Comment on the morphology of the red blood cells.
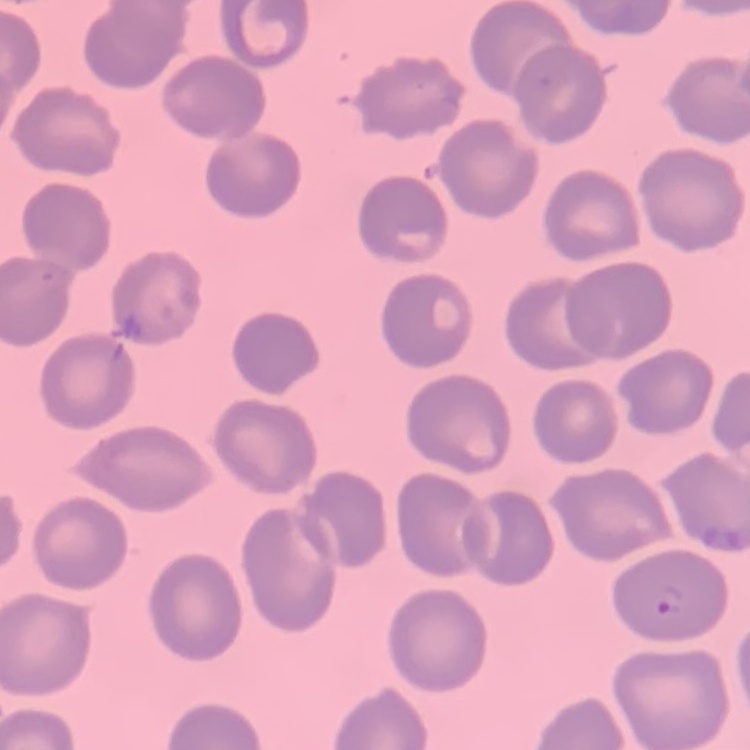

No rouleaux formation.

image type = one tile cut from a larger photomicrograph
preparation = thin blood smear
stain = Field's or Giemsa